Name the parasite shown.
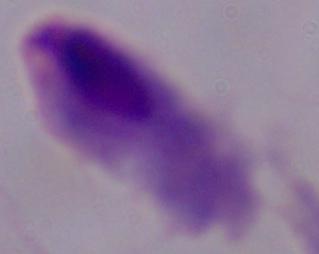

This is a trichomonad.

Summary:
  - Modality: photomicrograph
  - Magnification: 1000x